Outline every malaria parasite, every leukocyte, and every artifact (stain precipitate or debris).
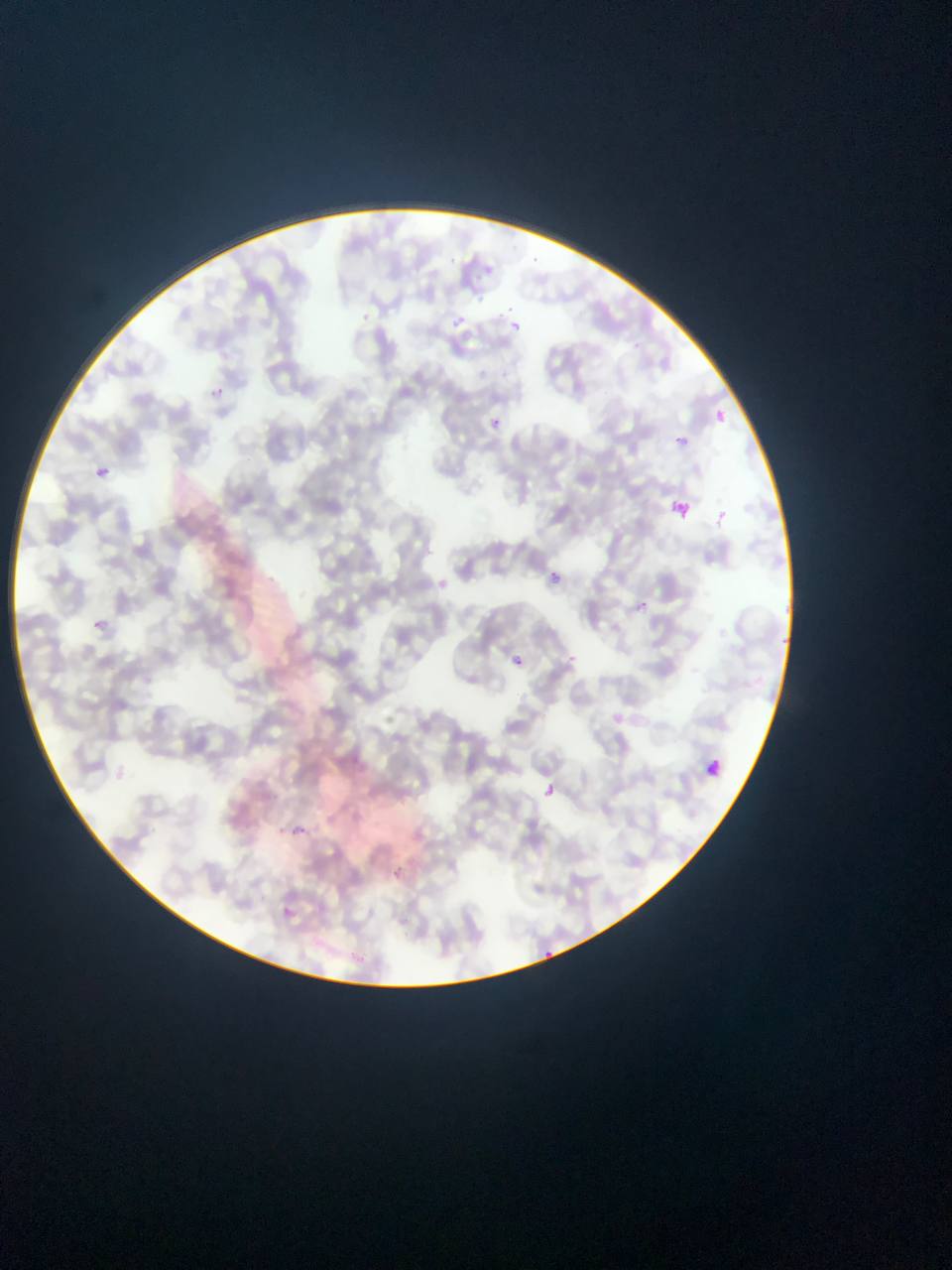

Approximate bounding boxes as (left, top, right, bottom) in pixels.
Malaria parasites: (535, 252, 547, 263), (506, 302, 516, 315), (356, 309, 373, 324), (452, 314, 468, 329), (510, 319, 522, 334), (206, 383, 231, 405), (709, 406, 731, 428), (485, 415, 502, 431), (670, 432, 693, 452), (90, 463, 112, 482), (667, 497, 693, 522), (717, 505, 729, 522), (549, 569, 565, 581), (640, 597, 651, 611), (91, 619, 105, 632), (500, 651, 530, 675), (569, 652, 579, 665), (707, 757, 725, 780), (535, 781, 561, 803), (292, 821, 312, 838), (395, 866, 406, 877), (540, 946, 552, 961).
No leukocytes observed.

Summary:
  - Image size: 952×1270 pixels
  - Field of view: single
  - Country: Ghana
  - Capture: mobile-phone photograph through a microscope
  - Preparation: thin blood smear